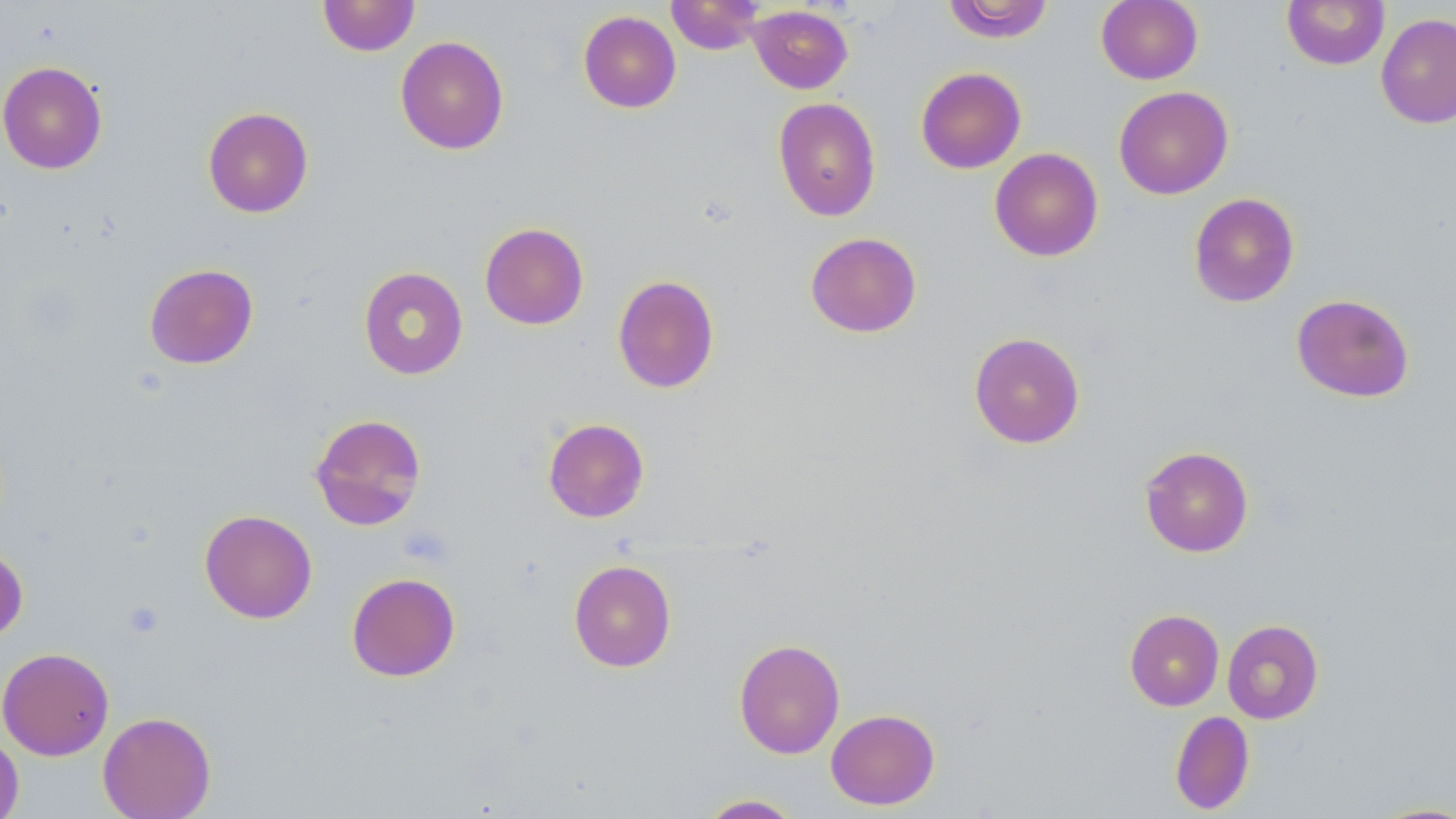

slide_level_diagnosis: negative for blood parasites
stain: May-Grünwald-Giemsa
modality: optical microscopy
image_size: 1456×819 pixels
magnification: 1000x
uninfected_red_blood_cell_locations: 'approximate bounding boxes as (x1,y1)-(x2,y2) corner pairs in pixels: (318,0)-(420,56), (666,0)-(765,54), (943,0)-(1055,42), (1096,0)-(1203,85), (1282,0)-(1390,70), (748,5)-(853,94), (578,10)-(681,113), (1376,13)-(1456,129), (395,35)-(509,155), (0,60)-(107,174), (915,67)-(1026,174), (1113,86)-(1233,199), (772,97)-(882,222), (203,106)-(314,218), (989,147)-(1104,262), (1188,192)-(1299,307), (479,222)-(589,330), (805,231)-(922,338), (144,263)-(258,369), (358,266)-(468,380), (612,274)-(719,393), (1291,293)-(1415,403), (968,331)-(1086,449), (309,413)-(427,530), (543,418)-(649,523), (1139,446)-(1254,557), (199,509)-(317,623), (0,544)-(28,644), (568,559)-(677,672), (346,572)-(460,681), (1125,609)-(1224,711), (1222,619)-(1324,724), (733,638)-(846,759), (0,647)-(115,760), (825,708)-(940,810), (1170,710)-(1255,814), (98,711)-(216,819), (0,730)-(24,819), (696,794)-(803,818), (1364,801)-(1456,818)'
preparation: thin blood film
field_of_view: one of a larger specimen
platelet_locations: 'approximate bounding boxes as (x1,y1)-(x2,y2) corner pairs in pixels: (399,525)-(453,568), (123,600)-(165,638)'